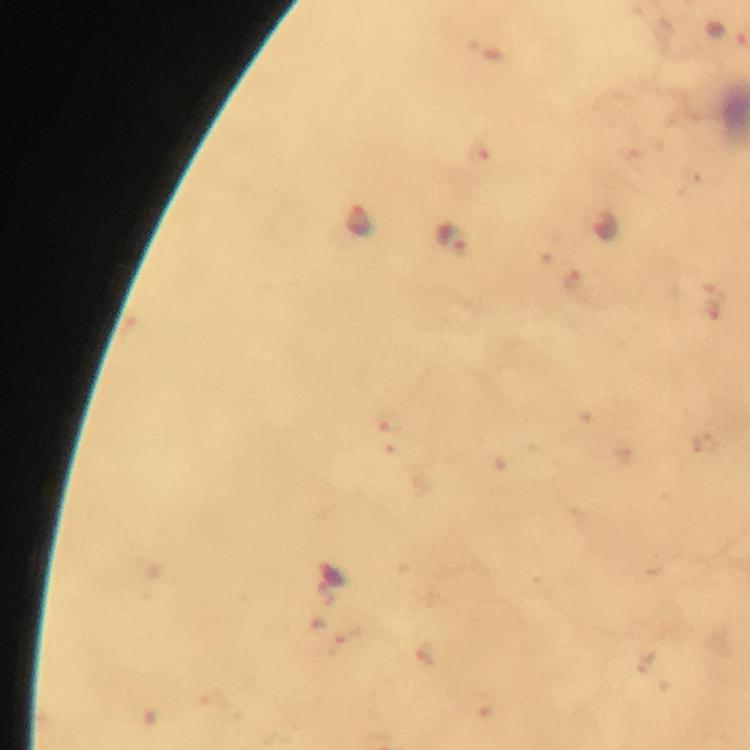

Approximate object centers, in pixels from the top-left corner. Plasmodium parasite locations: (x=723, y=35), (x=358, y=222), (x=606, y=225), (x=450, y=241). From a malaria diagnostic workup. Thick smear. Immersion oil was used. Giemsa stain. A crop from one field of view. Image is 750×750 pixels. At 100x magnification. Photographed through the microscope with a smartphone camera.